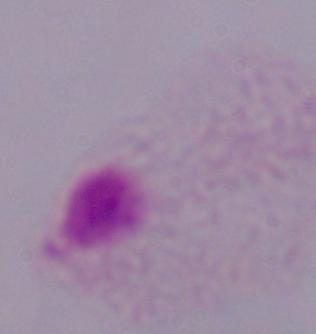
magnification = 1000x
identification = trichomonad
modality = photomicrograph